Locate every blood parasite and identify its species.
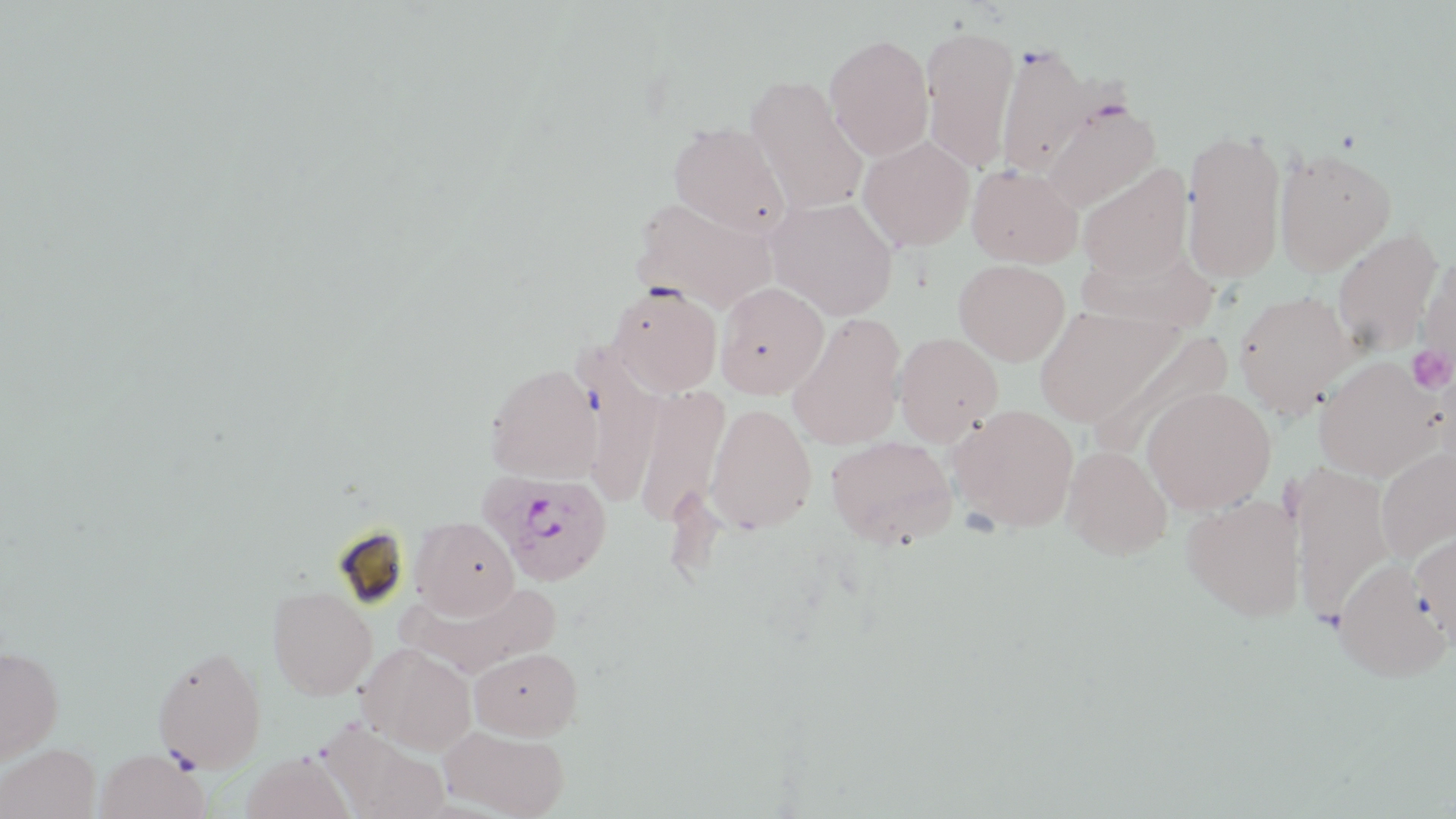
Approximate bounding boxes as named x1/y1/x2/y2 corners in pixels.
Plasmodium ovale-infected red blood cells: (x1=482, y1=470, x2=614, y2=586).
No Plasmodium falciparum, Plasmodium malariae, Plasmodium vivax, Babesia divergens, or Trypanosoma brucei observed.

slide-level diagnosis = Plasmodium ovale
image size = 1456×819 pixels
stain = May-Grünwald-Giemsa
platelet locations = approximate bounding boxes as named x1/y1/x2/y2 corners in pixels: (x1=1407, y1=345, x2=1454, y2=395)
modality = optical microscopy
field of view = single
preparation = thin blood smear
uninfected red blood cell locations = approximate bounding boxes as named x1/y1/x2/y2 corners in pixels: (x1=921, y1=26, x2=1019, y2=173), (x1=824, y1=33, x2=934, y2=161), (x1=995, y1=43, x2=1096, y2=178), (x1=746, y1=75, x2=869, y2=214), (x1=1040, y1=99, x2=1161, y2=213), (x1=668, y1=123, x2=792, y2=238), (x1=1181, y1=128, x2=1288, y2=281), (x1=858, y1=136, x2=975, y2=251), (x1=1274, y1=147, x2=1397, y2=276), (x1=1077, y1=162, x2=1193, y2=282), (x1=967, y1=164, x2=1084, y2=267), (x1=631, y1=196, x2=779, y2=312), (x1=766, y1=196, x2=899, y2=320), (x1=1331, y1=228, x2=1444, y2=354), (x1=1076, y1=242, x2=1218, y2=334), (x1=1417, y1=255, x2=1456, y2=382), (x1=954, y1=259, x2=1070, y2=365), (x1=714, y1=281, x2=829, y2=399), (x1=607, y1=282, x2=723, y2=396), (x1=1233, y1=289, x2=1358, y2=420), (x1=1034, y1=306, x2=1181, y2=428), (x1=786, y1=313, x2=907, y2=450), (x1=1088, y1=328, x2=1233, y2=460), (x1=893, y1=332, x2=1003, y2=446), (x1=574, y1=349, x2=664, y2=508), (x1=1312, y1=356, x2=1446, y2=481), (x1=484, y1=362, x2=603, y2=483), (x1=1430, y1=366, x2=1456, y2=484), (x1=632, y1=385, x2=730, y2=527), (x1=1142, y1=386, x2=1277, y2=514), (x1=705, y1=402, x2=817, y2=534), (x1=949, y1=403, x2=1080, y2=533), (x1=824, y1=435, x2=958, y2=549), (x1=1062, y1=444, x2=1172, y2=559), (x1=1374, y1=447, x2=1456, y2=563), (x1=1290, y1=462, x2=1394, y2=626), (x1=1181, y1=493, x2=1305, y2=621), (x1=411, y1=516, x2=519, y2=619), (x1=1410, y1=528, x2=1456, y2=650), (x1=1332, y1=558, x2=1452, y2=682), (x1=403, y1=580, x2=562, y2=680), (x1=266, y1=585, x2=377, y2=700), (x1=151, y1=643, x2=267, y2=774), (x1=359, y1=643, x2=477, y2=755), (x1=0, y1=645, x2=63, y2=765), (x1=470, y1=647, x2=582, y2=739), (x1=320, y1=722, x2=450, y2=819), (x1=439, y1=725, x2=570, y2=819), (x1=0, y1=741, x2=99, y2=818), (x1=94, y1=747, x2=209, y2=819), (x1=241, y1=752, x2=355, y2=819)
magnification = 1000x